Assess this cell for malaria.
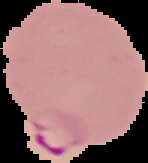

It is parasitized.

preparation: thin blood film
image_type: cell region segmented out of the field of view; surrounding area masked to black
image_size: 148×163 pixels